Assess this cell for malaria.
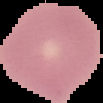
It is uninfected.

Image is 103×103 pixels. From a thin blood film. Cell region segmented out of the field of view; the surrounding area is masked to black.